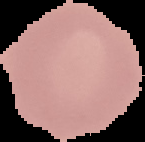
Malaria status: uninfected. Image is 145×142 pixels. The area outside the segmented cell region is set to black. From a thin blood film.